Assess this cell for malaria.
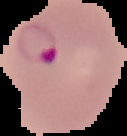

Parasitized.

Summary:
  - Image size: 127×136 pixels
  - Image type: segmented cell region on a black background
  - Preparation: thin blood smear